Outline each Plasmodium falciparum-infected red blood cell.
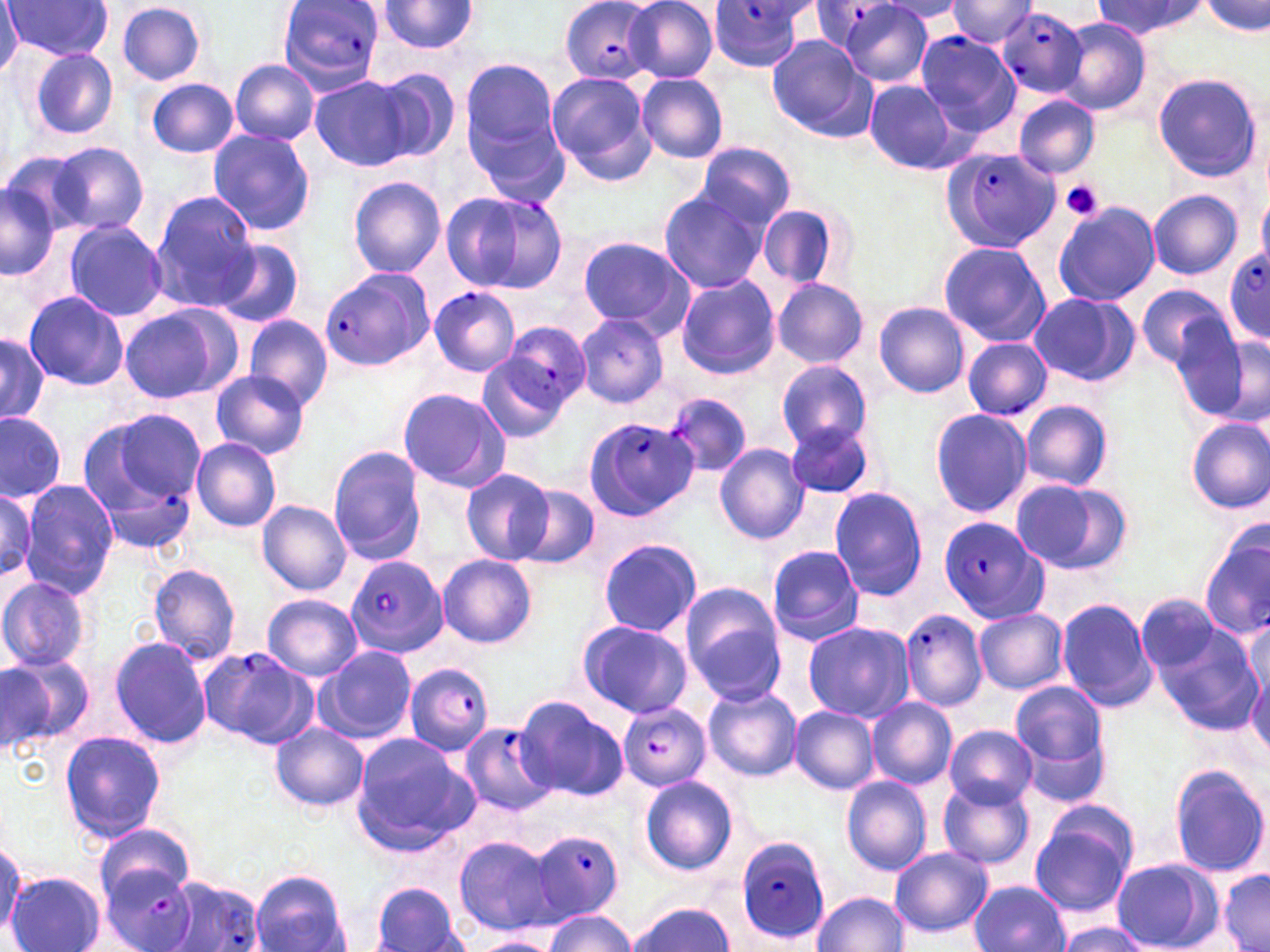

Approximate bounding boxes as (x1,y1)-(x2,y2) corner pairs in pixels.
Plasmodium falciparum-infected red blood cells: (277,0)-(385,93), (814,1)-(905,53), (561,2)-(659,82), (707,2)-(810,71), (997,7)-(1088,98), (914,31)-(1020,136), (944,147)-(1061,253), (439,190)-(566,296), (1224,246)-(1270,344), (319,269)-(430,373), (429,285)-(520,376), (504,322)-(590,410), (581,418)-(697,521), (103,475)-(197,551), (938,515)-(1048,623), (348,555)-(447,657), (900,610)-(989,712), (199,646)-(317,748), (404,663)-(494,754), (619,703)-(711,791), (458,720)-(556,816), (528,830)-(626,920), (735,838)-(830,943), (99,864)-(198,952), (160,876)-(265,952).

slide-level diagnosis = Plasmodium falciparum
magnification = 1000x
preparation = thin blood film
image size = 1270×952 pixels
modality = light microscopy
stain = May-Grünwald-Giemsa
uninfected red blood cell locations = approximate bounding boxes as (x1,y1)-(x2,y2) corner pairs in pixels: (625,0)-(719,82), (3,1)-(113,61), (947,1)-(1038,48), (1094,1)-(1204,39), (1202,1)-(1270,36), (116,2)-(207,85), (377,2)-(480,56), (842,2)-(937,86), (0,7)-(26,73), (1057,18)-(1149,115), (766,34)-(873,139), (28,48)-(120,139), (461,56)-(568,181), (230,60)-(319,145), (371,67)-(461,165), (545,70)-(655,186), (1151,72)-(1266,184), (636,73)-(729,163), (311,74)-(413,172), (145,77)-(239,159), (862,80)-(964,174), (1014,95)-(1100,177), (207,129)-(317,236), (50,142)-(147,234), (695,143)-(797,229), (2,152)-(86,244), (348,176)-(446,278), (0,177)-(60,280), (657,189)-(769,293), (1148,189)-(1242,279), (150,190)-(258,303), (1053,200)-(1161,307), (757,202)-(846,289), (62,219)-(167,321), (575,236)-(696,337), (211,238)-(305,328), (938,241)-(1051,346), (673,275)-(780,381), (772,278)-(869,368), (1138,284)-(1231,370), (23,291)-(129,391), (1029,291)-(1139,388), (873,302)-(970,397), (119,303)-(237,405), (573,313)-(668,406), (243,314)-(333,410), (1168,321)-(1254,418), (1180,322)-(1267,507), (0,333)-(49,422), (1210,333)-(1270,425), (962,338)-(1052,419), (476,349)-(576,444), (776,358)-(872,449), (210,369)-(312,459), (396,387)-(511,491), (669,393)-(753,477), (1020,400)-(1114,491), (87,407)-(206,497), (930,408)-(1032,518), (0,411)-(67,503), (783,417)-(880,501), (1186,417)-(1270,512), (191,437)-(282,532), (715,443)-(810,545), (327,447)-(426,563), (461,469)-(554,564), (18,479)-(119,597), (1009,479)-(1133,576), (513,486)-(600,568), (0,488)-(37,579), (829,488)-(927,601), (257,500)-(352,595), (1199,531)-(1270,640), (598,538)-(702,639), (767,545)-(864,646), (436,555)-(537,649), (146,562)-(243,665), (0,576)-(93,671), (679,585)-(785,702), (262,595)-(363,681), (1137,595)-(1222,677), (1057,597)-(1158,711), (975,607)-(1069,695), (1149,614)-(1264,736), (577,620)-(693,719), (1245,620)-(1268,703), (803,621)-(916,722), (109,635)-(213,749), (314,647)-(416,744), (7,652)-(96,743), (0,658)-(57,756), (1246,659)-(1270,759), (1010,681)-(1106,772), (703,686)-(802,781), (514,696)-(628,801), (866,697)-(957,789), (789,705)-(880,795), (1016,720)-(1113,808), (269,723)-(368,813), (943,726)-(1038,807), (59,731)-(165,842), (350,734)-(475,855), (1168,765)-(1269,878), (841,776)-(932,875), (640,777)-(738,877), (939,782)-(1035,870), (1030,806)-(1138,915), (95,825)-(195,908), (454,835)-(555,934), (0,844)-(24,938), (889,846)-(992,939), (1109,858)-(1221,951), (1217,869)-(1269,952), (251,870)-(351,952), (8,872)-(104,952), (968,881)-(1069,952), (372,883)-(468,952), (812,891)-(909,951), (623,901)-(738,951), (543,909)-(636,952), (1054,921)-(1152,952), (472,934)-(563,952)
platelet locations = approximate bounding boxes as (x1,y1)-(x2,y2) corner pairs in pixels: (1059,180)-(1106,222)
field of view = one of a larger specimen